Report the malaria status of this cell.
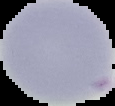
Uninfected.

preparation: thin blood smear
image_type: segmented cell region with the area outside set to black
image_size: 115×106 pixels